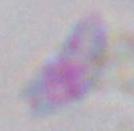

Captured at 1000x magnification. Toxoplasma gondii is seen. Photomicrograph.